Identify the parasite.
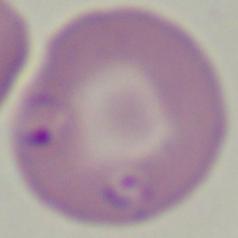
Babesia.

{
  "magnification": "1000x",
  "modality": "photomicrograph"
}